Describe the morphology of the erythrocytes.
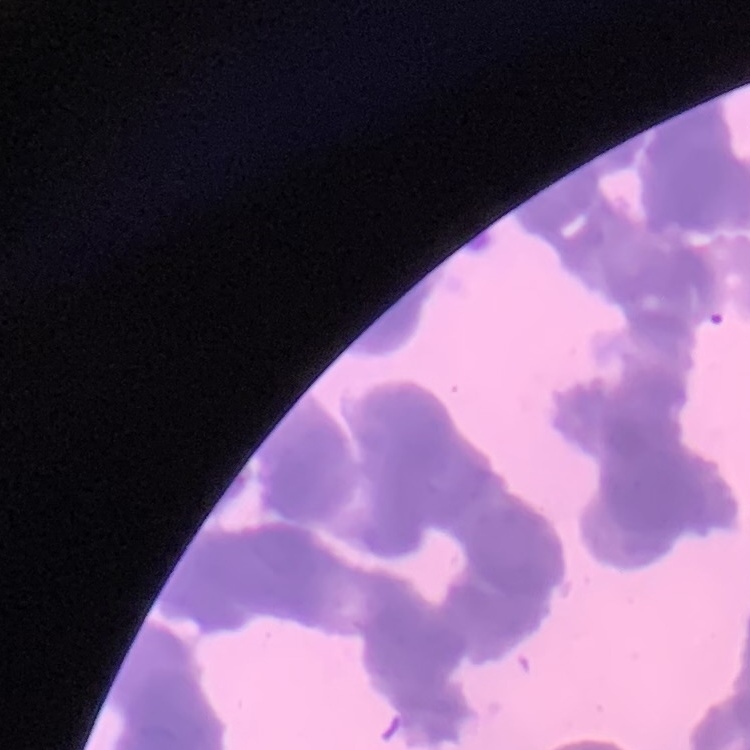

They show rouleaux formation.

Thin peripheral smear. Field's or Giemsa stain. One tile cut from a larger photomicrograph.